Report the malaria status of this cell.
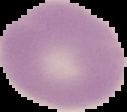

It is uninfected.

Summary:
  - Image size: 127×112 pixels
  - Preparation: thin blood smear
  - Image type: cell region segmented out of the field of view; surrounding area masked to black